Outline platelets.
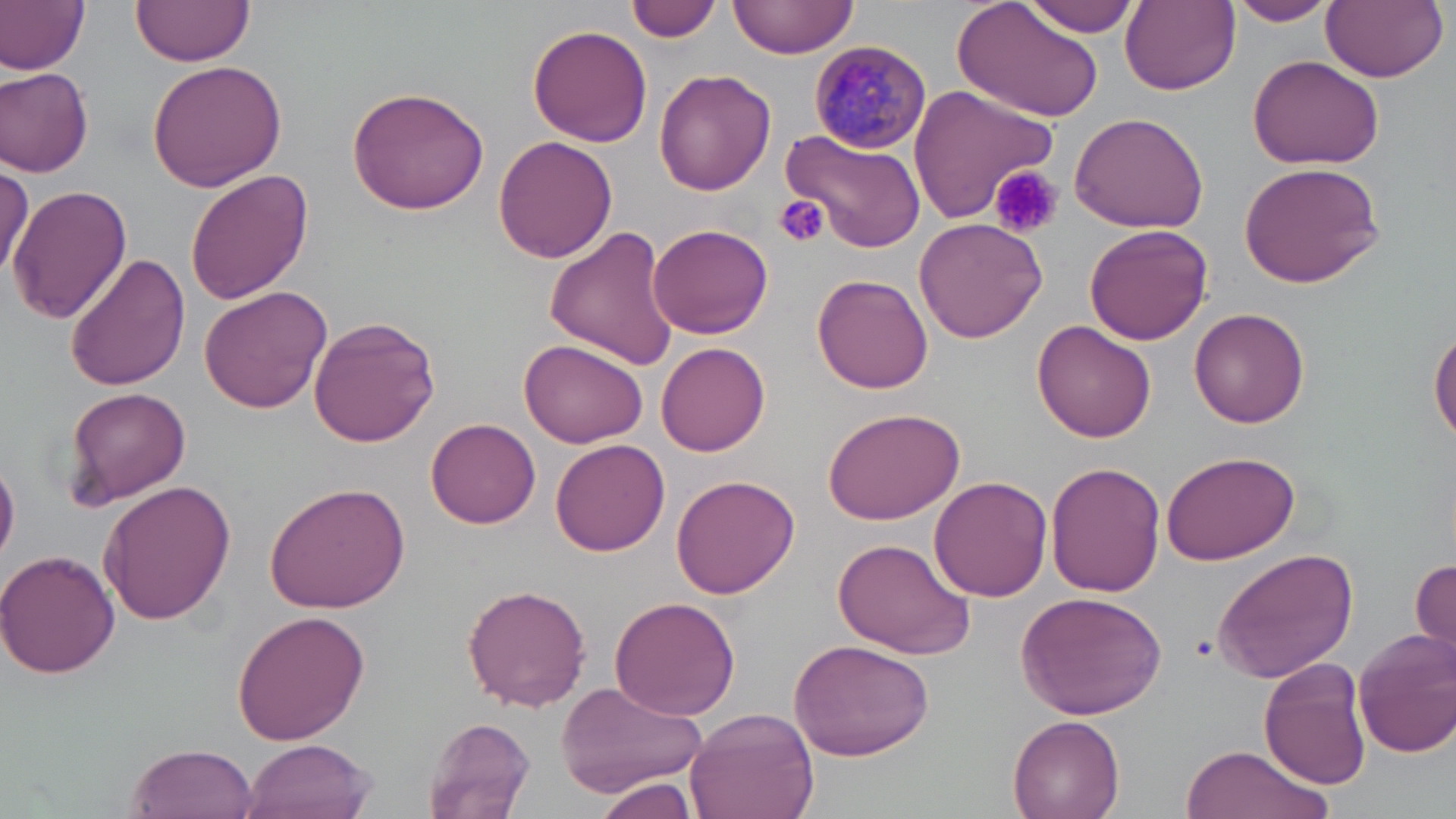
Approximate bounding boxes as named x1/y1/x2/y2 corners in pixels.
Platelets: (x1=991, y1=167, x2=1063, y2=241), (x1=774, y1=194, x2=830, y2=248).

Plasmodium malariae-infected red blood cell locations: (x1=810, y1=38, x2=932, y2=154). Uninfected red blood cell locations: (x1=0, y1=0, x2=90, y2=75), (x1=129, y1=0, x2=256, y2=70), (x1=626, y1=0, x2=720, y2=43), (x1=725, y1=0, x2=860, y2=65), (x1=952, y1=0, x2=1105, y2=127), (x1=1019, y1=0, x2=1142, y2=36), (x1=1227, y1=0, x2=1336, y2=26), (x1=1321, y1=0, x2=1448, y2=82), (x1=1121, y1=1, x2=1240, y2=95), (x1=528, y1=25, x2=654, y2=148), (x1=1247, y1=55, x2=1385, y2=169), (x1=147, y1=58, x2=290, y2=192), (x1=0, y1=68, x2=94, y2=178), (x1=655, y1=68, x2=776, y2=194), (x1=906, y1=84, x2=1056, y2=223), (x1=346, y1=86, x2=491, y2=214), (x1=1068, y1=109, x2=1210, y2=233), (x1=784, y1=128, x2=926, y2=253), (x1=493, y1=136, x2=617, y2=263), (x1=0, y1=163, x2=31, y2=282), (x1=1238, y1=163, x2=1386, y2=288), (x1=184, y1=168, x2=314, y2=305), (x1=5, y1=183, x2=131, y2=323), (x1=913, y1=216, x2=1048, y2=343), (x1=649, y1=223, x2=773, y2=339), (x1=544, y1=224, x2=683, y2=369), (x1=1084, y1=224, x2=1213, y2=345), (x1=64, y1=252, x2=191, y2=392), (x1=811, y1=273, x2=934, y2=394), (x1=198, y1=285, x2=331, y2=412), (x1=1190, y1=307, x2=1310, y2=427), (x1=307, y1=315, x2=441, y2=446), (x1=1033, y1=321, x2=1158, y2=443), (x1=1429, y1=326, x2=1456, y2=443), (x1=520, y1=340, x2=648, y2=449), (x1=658, y1=342, x2=771, y2=458), (x1=64, y1=386, x2=192, y2=508), (x1=823, y1=408, x2=965, y2=525), (x1=426, y1=417, x2=541, y2=528), (x1=551, y1=436, x2=670, y2=556), (x1=1161, y1=450, x2=1300, y2=564), (x1=0, y1=456, x2=20, y2=567), (x1=1045, y1=460, x2=1164, y2=597), (x1=670, y1=474, x2=800, y2=601), (x1=928, y1=477, x2=1053, y2=604), (x1=265, y1=480, x2=411, y2=614), (x1=99, y1=481, x2=236, y2=625), (x1=832, y1=535, x2=975, y2=658), (x1=1213, y1=546, x2=1359, y2=684), (x1=0, y1=548, x2=122, y2=681), (x1=1411, y1=554, x2=1456, y2=661), (x1=463, y1=584, x2=592, y2=713), (x1=1015, y1=592, x2=1169, y2=720), (x1=609, y1=596, x2=742, y2=720), (x1=232, y1=609, x2=369, y2=745), (x1=1352, y1=626, x2=1456, y2=756), (x1=787, y1=639, x2=935, y2=759), (x1=1261, y1=657, x2=1375, y2=790), (x1=551, y1=680, x2=707, y2=802), (x1=684, y1=708, x2=820, y2=819), (x1=1007, y1=713, x2=1126, y2=819), (x1=424, y1=716, x2=537, y2=819), (x1=240, y1=738, x2=376, y2=819), (x1=126, y1=743, x2=260, y2=819), (x1=1181, y1=744, x2=1328, y2=819), (x1=594, y1=778, x2=700, y2=819). Slide-level diagnosis: Plasmodium malariae. Light microscopy. Thin blood smear. 1000x magnification. Single field of view. May-Grünwald-Giemsa stain. Image is 1456×819 pixels.